Classify this cell by malaria status.
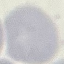

It is uninfected.

stain = Giemsa
image type = cell patch, automatically extracted from a larger field of view and resized to 64 × 64 pixels
capture = smartphone camera at the microscope eyepiece
preparation = thin blood smear